Give the position of every Plasmodium parasite visible.
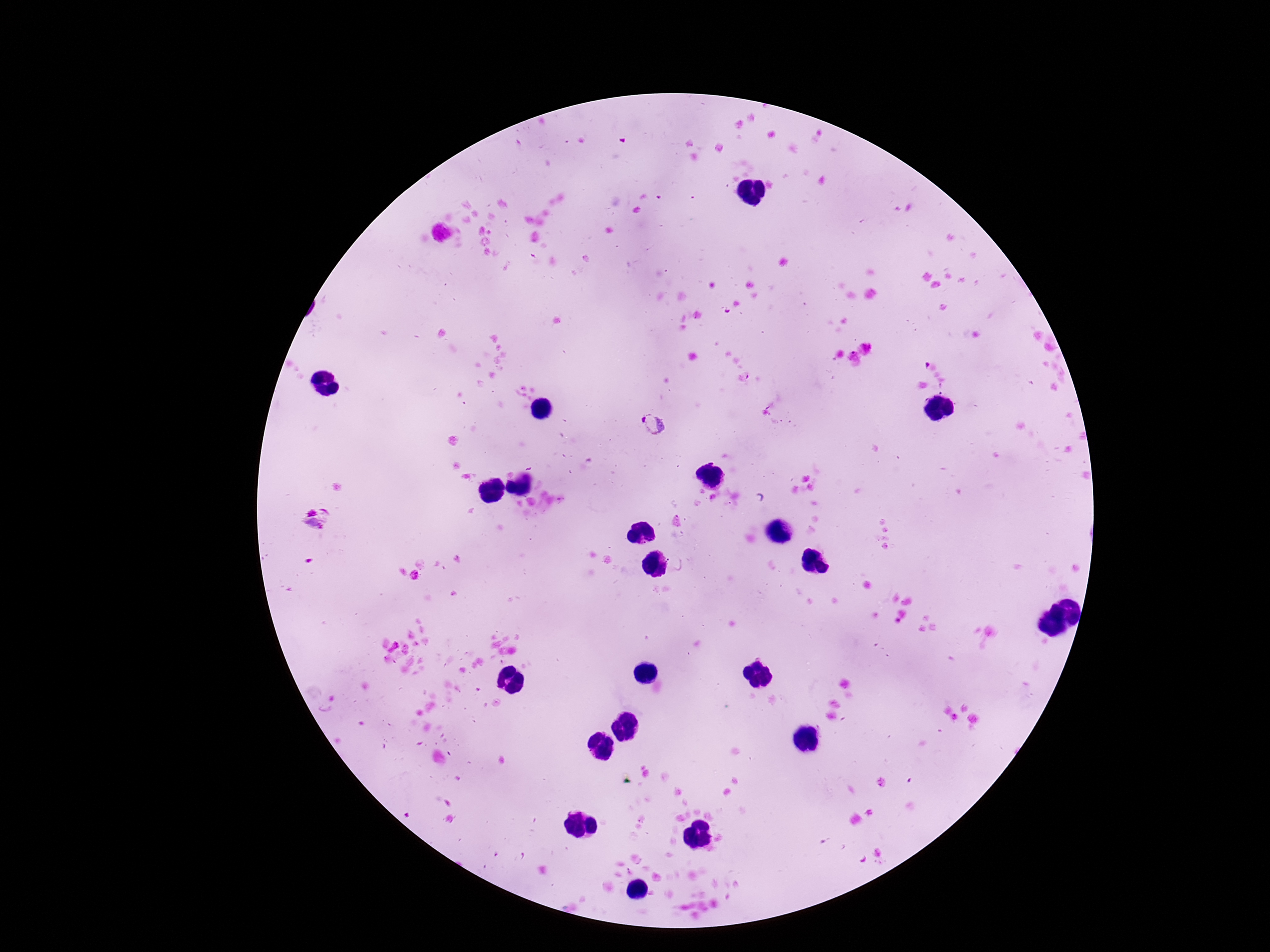

Approximate centers as [x, y] in pixels.
Plasmodium parasites: [653, 426].

{
  "patient_malaria_status": "infected",
  "field_of_view": "single",
  "capture": "smartphone camera through the microscope eyepiece",
  "image_size": "1270×952 pixels",
  "stain": "Giemsa",
  "magnification": "100x",
  "preparation": "thick blood film"
}